Identify the parasite.
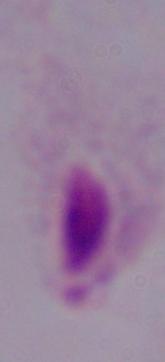

This is a trichomonad.

Summary:
  - Magnification: 1000x
  - Modality: micrograph